Locate every uninfected red blood cell.
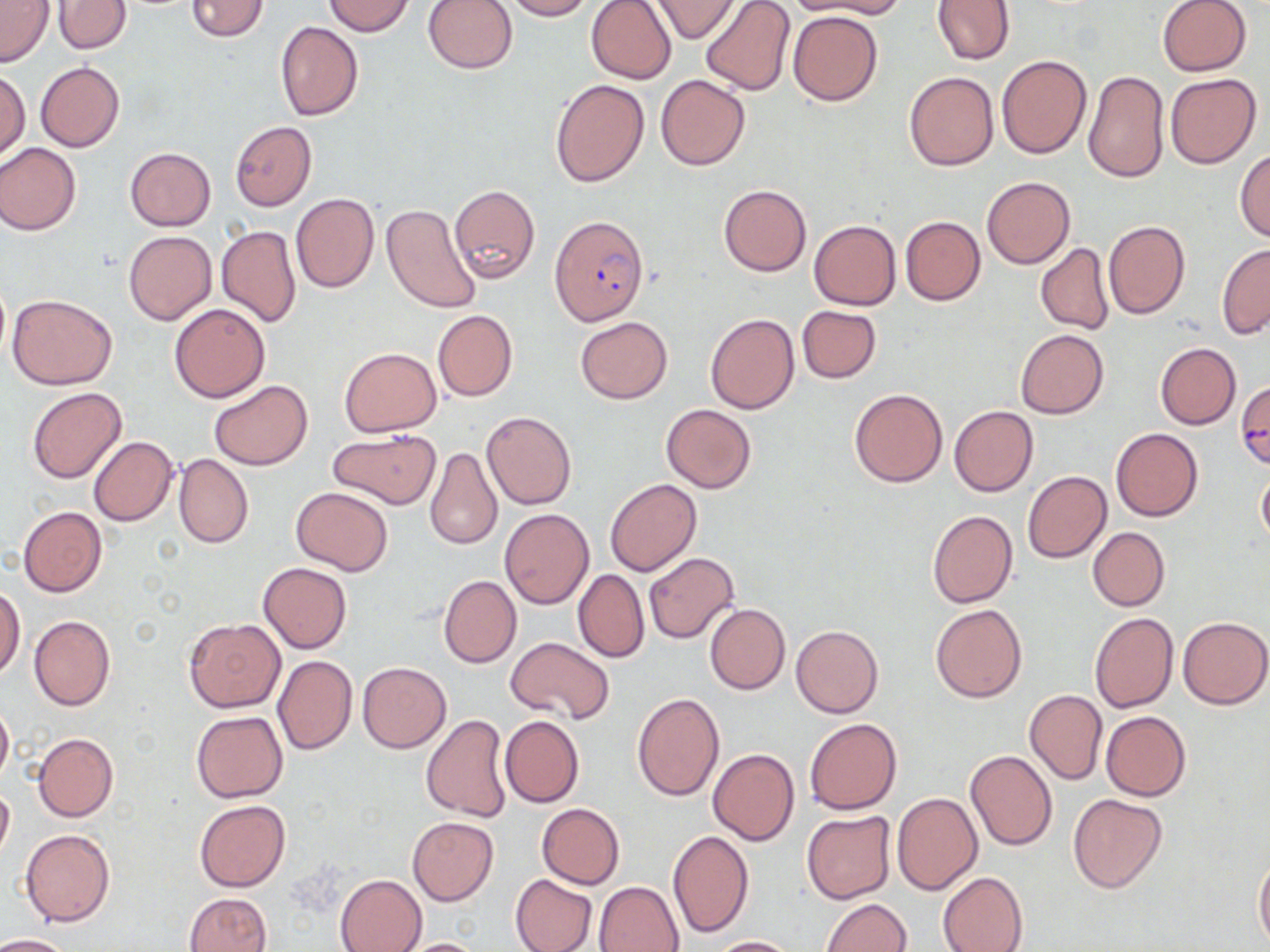
Approximate bounding boxes as (x1, y1, x2, y2) in pixels.
Uninfected red blood cells: (1, 0, 54, 68), (185, 0, 268, 41), (423, 0, 518, 74), (499, 0, 594, 20), (650, 0, 739, 42), (701, 0, 794, 97), (794, 0, 908, 19), (931, 0, 1015, 64), (1156, 0, 1252, 76), (322, 1, 414, 36), (586, 1, 676, 84), (51, 2, 131, 55), (788, 10, 882, 105), (276, 21, 363, 121), (996, 54, 1091, 159), (36, 62, 124, 152), (0, 70, 30, 162), (1083, 70, 1169, 183), (904, 72, 998, 171), (1165, 73, 1262, 169), (656, 75, 750, 170), (549, 78, 649, 188), (230, 121, 317, 210), (0, 143, 80, 235), (125, 148, 215, 230), (1234, 149, 1270, 242), (981, 177, 1074, 268), (449, 183, 540, 286), (719, 184, 811, 277), (292, 193, 379, 293), (381, 205, 481, 313), (900, 215, 985, 305), (809, 220, 901, 310), (1103, 220, 1190, 320), (216, 226, 302, 328), (124, 230, 216, 325), (1216, 243, 1270, 339), (1036, 244, 1114, 335), (7, 294, 116, 390), (169, 303, 271, 403), (796, 305, 882, 384), (432, 308, 517, 402), (705, 312, 800, 414), (575, 317, 672, 404), (1015, 329, 1108, 419), (1155, 342, 1241, 430), (339, 347, 442, 436), (209, 380, 313, 469), (26, 387, 126, 484), (849, 388, 947, 487), (660, 404, 757, 493), (948, 405, 1038, 496), (481, 410, 577, 511), (1110, 428, 1203, 521), (328, 429, 441, 509), (88, 436, 177, 526), (425, 446, 504, 551), (173, 453, 254, 548), (1257, 467, 1270, 549), (1022, 471, 1112, 563), (605, 479, 702, 576), (291, 486, 394, 576), (18, 506, 107, 597), (499, 509, 594, 609), (927, 510, 1017, 608), (1087, 527, 1170, 611), (644, 552, 739, 644), (258, 562, 351, 653), (573, 568, 649, 663), (439, 576, 521, 668), (1, 584, 25, 679), (705, 603, 790, 694), (931, 604, 1027, 703), (1089, 611, 1177, 713), (29, 616, 115, 710), (1178, 616, 1270, 709), (184, 619, 285, 712), (792, 624, 883, 718), (505, 637, 615, 725), (272, 654, 357, 755), (357, 662, 451, 752), (1024, 689, 1108, 785), (631, 692, 724, 802), (0, 701, 13, 787), (191, 711, 288, 803), (1101, 711, 1192, 802), (421, 714, 511, 822), (500, 716, 584, 807), (805, 718, 901, 815), (33, 733, 118, 821), (708, 749, 800, 847), (965, 749, 1057, 851), (0, 784, 14, 864), (891, 792, 982, 895), (1068, 794, 1167, 894), (194, 800, 290, 892), (536, 803, 625, 889), (802, 811, 897, 904), (407, 817, 498, 905), (20, 829, 115, 927), (669, 830, 754, 938), (1254, 854, 1270, 948), (938, 871, 1028, 952), (335, 874, 427, 952), (509, 874, 598, 952), (594, 880, 684, 951), (184, 893, 271, 952), (819, 898, 911, 951), (0, 933, 76, 952), (706, 935, 803, 952), (392, 938, 490, 951).

slide-level diagnosis = Plasmodium falciparum
magnification = 1000x
Plasmodium falciparum-infected red blood cell locations = approximate bounding boxes as (x1, y1, x2, y2) in pixels: (549, 216, 649, 325)
preparation = thin blood smear
stain = May-Grünwald-Giemsa
modality = optical microscopy
image size = 1270×952 pixels
field of view = single